Assess this cell for malaria.
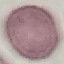

Uninfected.

Summary:
  - Image type: cell patch, automatically extracted from a larger field of view and resized to 64 × 64 pixels
  - Stain: Giemsa
  - Capture: smartphone camera at the microscope eyepiece
  - Preparation: thin blood film